Locate and identify every blood parasite.
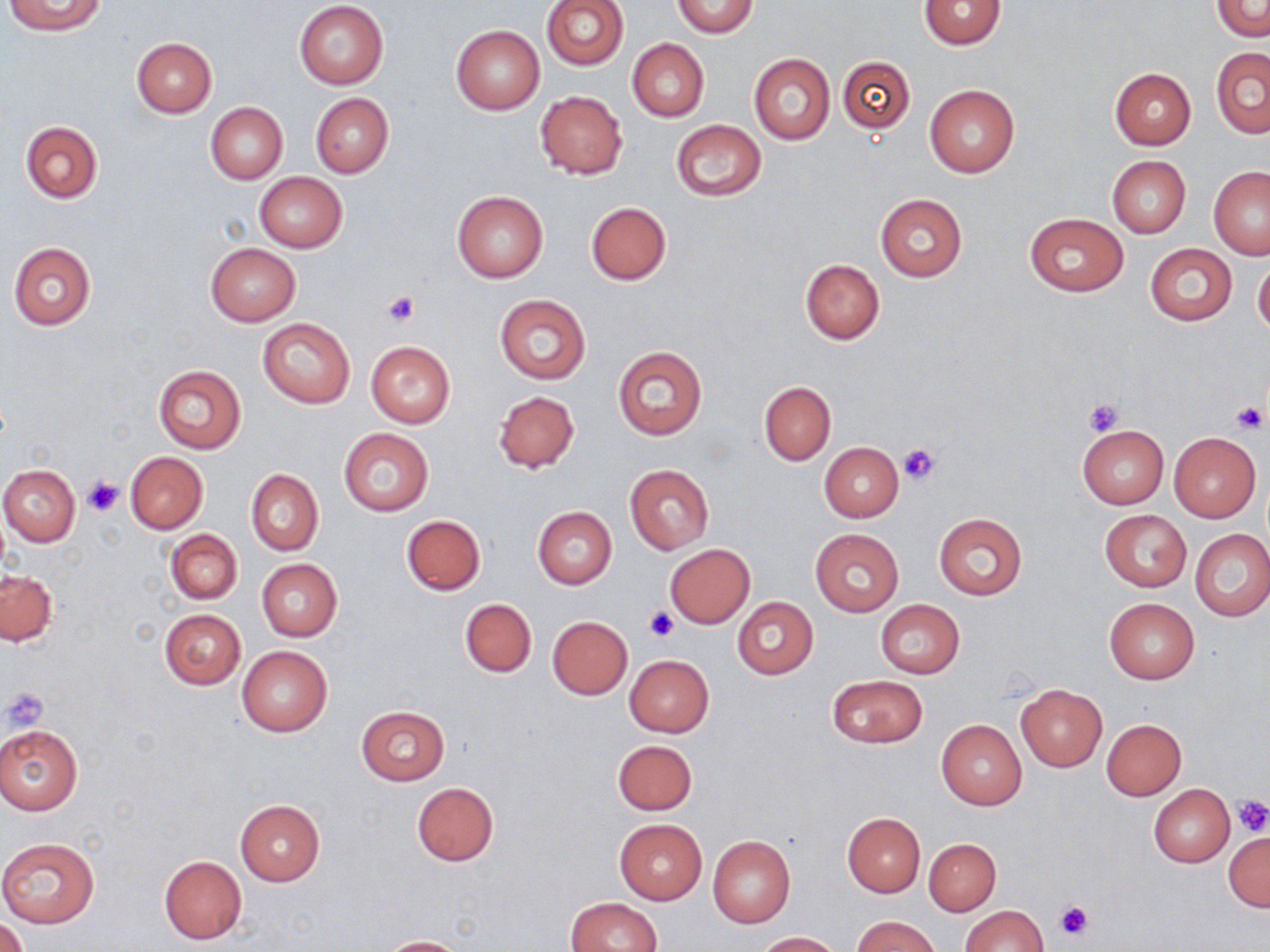

No blood parasites seen.

{
  "slide_level_diagnosis": "negative for blood parasites",
  "field_of_view": "single",
  "image_size": "1270×952 pixels",
  "uninfected_red_blood_cell_locations": "approximate bounding boxes as [x1, y1, x2, y2] in pixels: [4, 0, 107, 35], [672, 0, 759, 38], [539, 1, 628, 70], [919, 1, 1006, 50], [1211, 1, 1270, 40], [294, 2, 389, 89], [450, 25, 544, 114], [131, 36, 217, 117], [628, 38, 708, 121], [1211, 49, 1269, 138], [748, 53, 835, 145], [837, 56, 915, 133], [1110, 67, 1196, 149], [924, 84, 1019, 178], [534, 90, 628, 179], [310, 92, 393, 178], [205, 102, 287, 185], [670, 120, 766, 200], [19, 121, 103, 204], [1107, 155, 1190, 237], [1209, 166, 1270, 258], [254, 172, 347, 252], [452, 190, 549, 284], [876, 194, 967, 281], [585, 202, 670, 285], [1023, 213, 1129, 296], [8, 242, 96, 329], [205, 243, 300, 325], [1144, 244, 1237, 325], [800, 258, 885, 344], [1253, 259, 1270, 337], [495, 295, 590, 384], [258, 318, 355, 408], [365, 340, 456, 428], [612, 345, 708, 441], [153, 365, 246, 453], [759, 381, 836, 465], [493, 391, 579, 475], [1077, 424, 1168, 508], [338, 427, 434, 515], [1168, 432, 1261, 522], [819, 442, 903, 522], [125, 452, 208, 533], [0, 465, 80, 546], [625, 465, 713, 554], [245, 469, 322, 556], [532, 506, 616, 588], [1100, 510, 1191, 591], [934, 513, 1025, 600], [402, 515, 485, 595], [165, 529, 242, 603], [1191, 529, 1270, 621], [812, 530, 903, 614], [665, 544, 755, 628], [256, 559, 341, 641], [1, 569, 57, 646], [459, 598, 536, 676], [732, 598, 818, 678], [1104, 598, 1199, 683], [876, 600, 965, 678], [159, 609, 246, 690], [547, 616, 632, 699], [236, 646, 332, 737], [625, 654, 714, 737], [828, 675, 928, 747], [1016, 686, 1106, 770], [355, 706, 449, 785], [1101, 719, 1187, 800], [936, 720, 1027, 810], [0, 723, 83, 815], [613, 740, 697, 815], [412, 783, 498, 866], [1149, 784, 1234, 866], [235, 800, 324, 885], [842, 814, 925, 897], [614, 819, 707, 904], [1223, 831, 1270, 912], [707, 836, 795, 928], [0, 838, 102, 928], [924, 838, 1000, 916], [159, 856, 246, 945], [566, 897, 661, 951], [959, 905, 1048, 952], [850, 915, 940, 952], [0, 918, 29, 952], [754, 931, 842, 951], [378, 936, 468, 951]",
  "platelet_locations": "approximate bounding boxes as [x1, y1, x2, y2] in pixels: [381, 291, 419, 327], [1083, 397, 1124, 437], [1231, 402, 1267, 433], [897, 443, 940, 486], [82, 476, 125, 517], [645, 605, 679, 641], [4, 687, 48, 732], [1231, 795, 1270, 836], [1055, 900, 1092, 941]",
  "magnification": "1000x",
  "stain": "May-Grünwald-Giemsa",
  "preparation": "thin blood film",
  "modality": "optical microscopy"
}